Assess this cell for malaria.
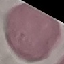

Uninfected.

Thin blood film. Giemsa stain. Photographed with a smartphone camera at the microscope eyepiece. Cell patch, automatically extracted from a larger field of view and resized to 64 × 64 pixels.